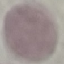

Summary:
  - Malaria status: uninfected
  - Stain: Giemsa
  - Image type: automatically extracted cell patch, resized to 64 × 64 pixels
  - Preparation: thin smear
  - Capture: smartphone camera at the microscope eyepiece